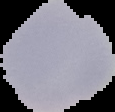

image size = 115×112 pixels
malaria status = uninfected
preparation = thin blood film
image type = segmented cell region with the area outside set to black